Identify the parasite.
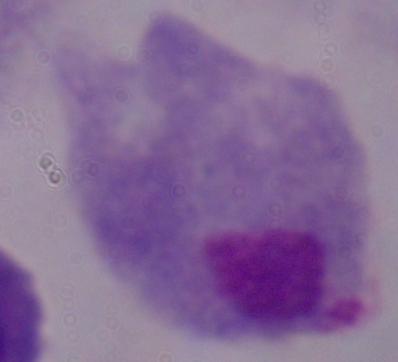
A trichomonad.

Summary:
  - Magnification: 1000x
  - Modality: photomicrograph